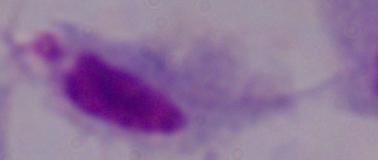
Summary:
  - Magnification: 1000x
  - Modality: photomicrograph
  - Identification: trichomonad